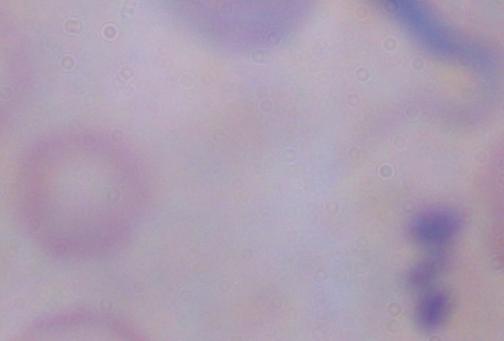
{
  "magnification": "1000x",
  "modality": "photomicrograph",
  "identification": "trypanosome"
}